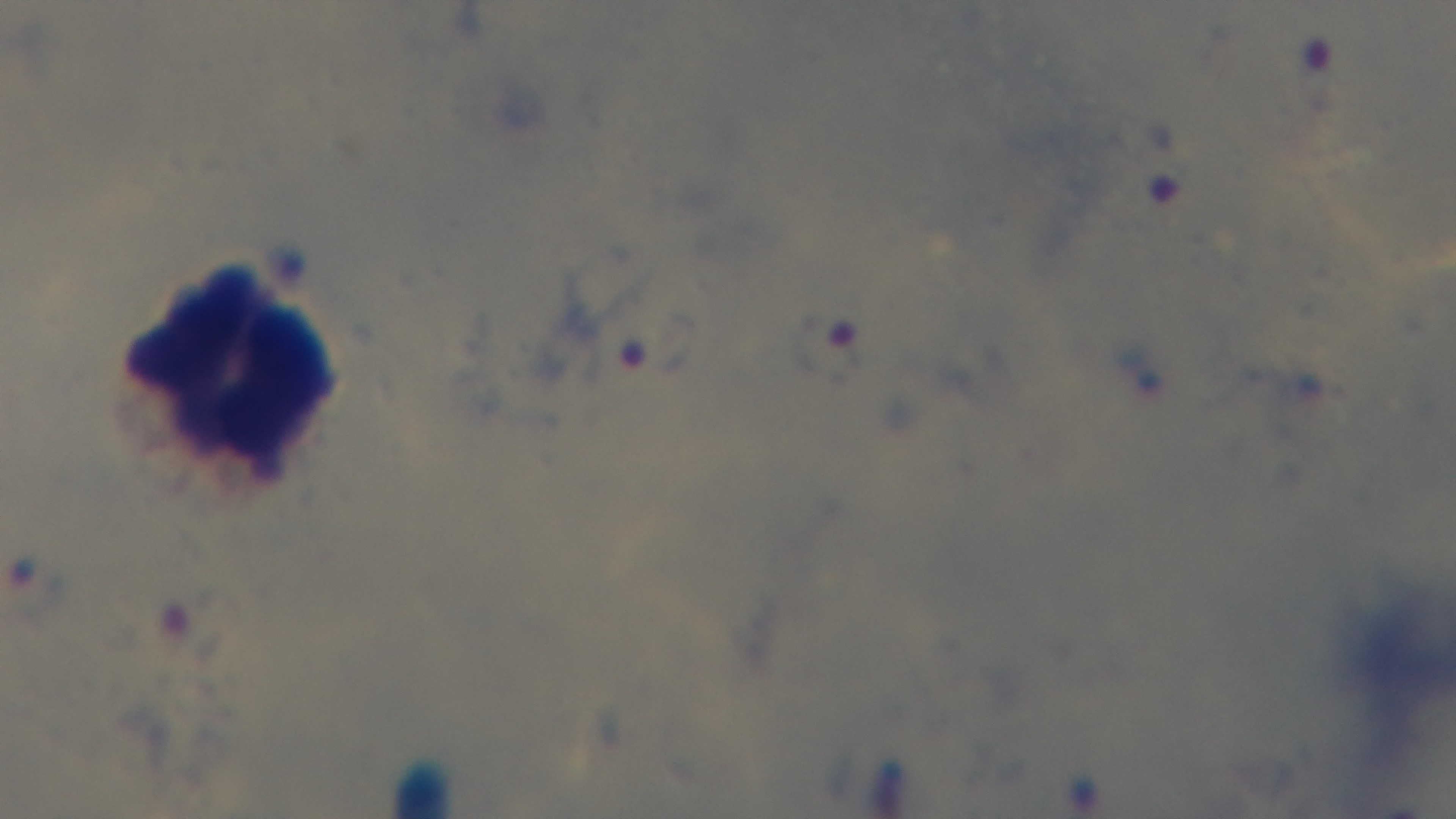

Summary:
  - Objective: 100x oil immersion
  - Field of view: one from the slide
  - Preparation: thick smear
  - Capture: mounted 4K digital camera
  - Stain: Giemsa
  - Modality: light microscopy
  - Malaria status: positive